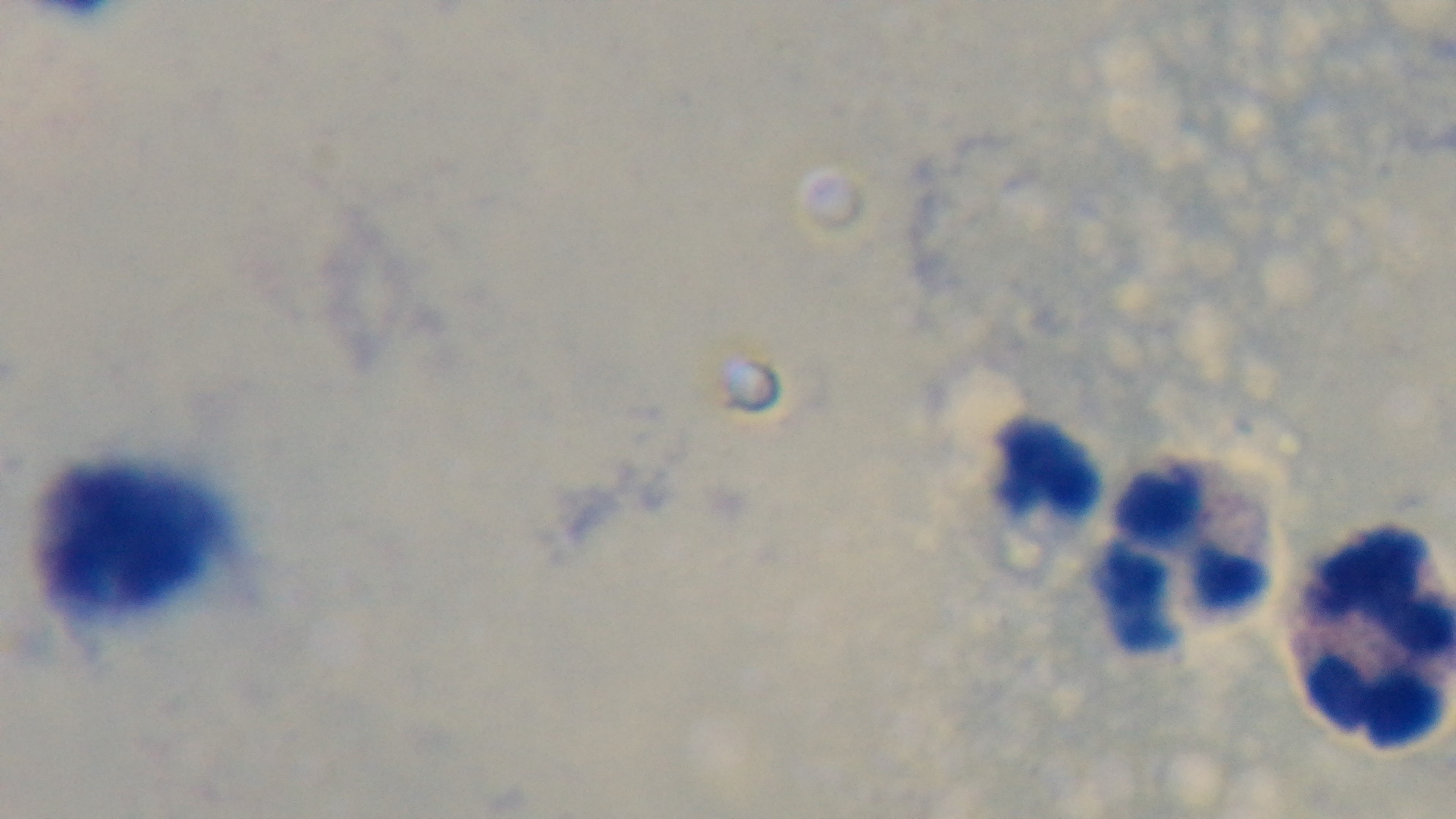
Summary:
  - Preparation: thick blood film
  - Malaria status: negative
  - Capture: mounted 4K digital camera
  - Field of view: single
  - Stain: Giemsa
  - Modality: light microscopy
  - Objective: 100x oil immersion